Classify this cell by malaria status.
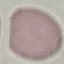
Uninfected.

Thin blood smear. Automatically extracted cell patch, resized to 64 × 64 pixels. Photographed with a smartphone camera at the microscope eyepiece. Giemsa stain.